Classify this cell by malaria status.
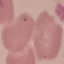
Uninfected.

Summary:
  - Image type: cell patch, automatically extracted from a larger field of view and resized to 64 × 64 pixels
  - Stain: Giemsa
  - Preparation: thin blood smear
  - Capture: smartphone through the microscope eyepiece